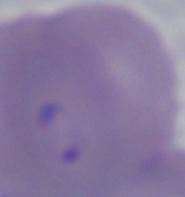
{
  "modality": "photomicrograph",
  "identification": "Babesia",
  "magnification": "1000x"
}